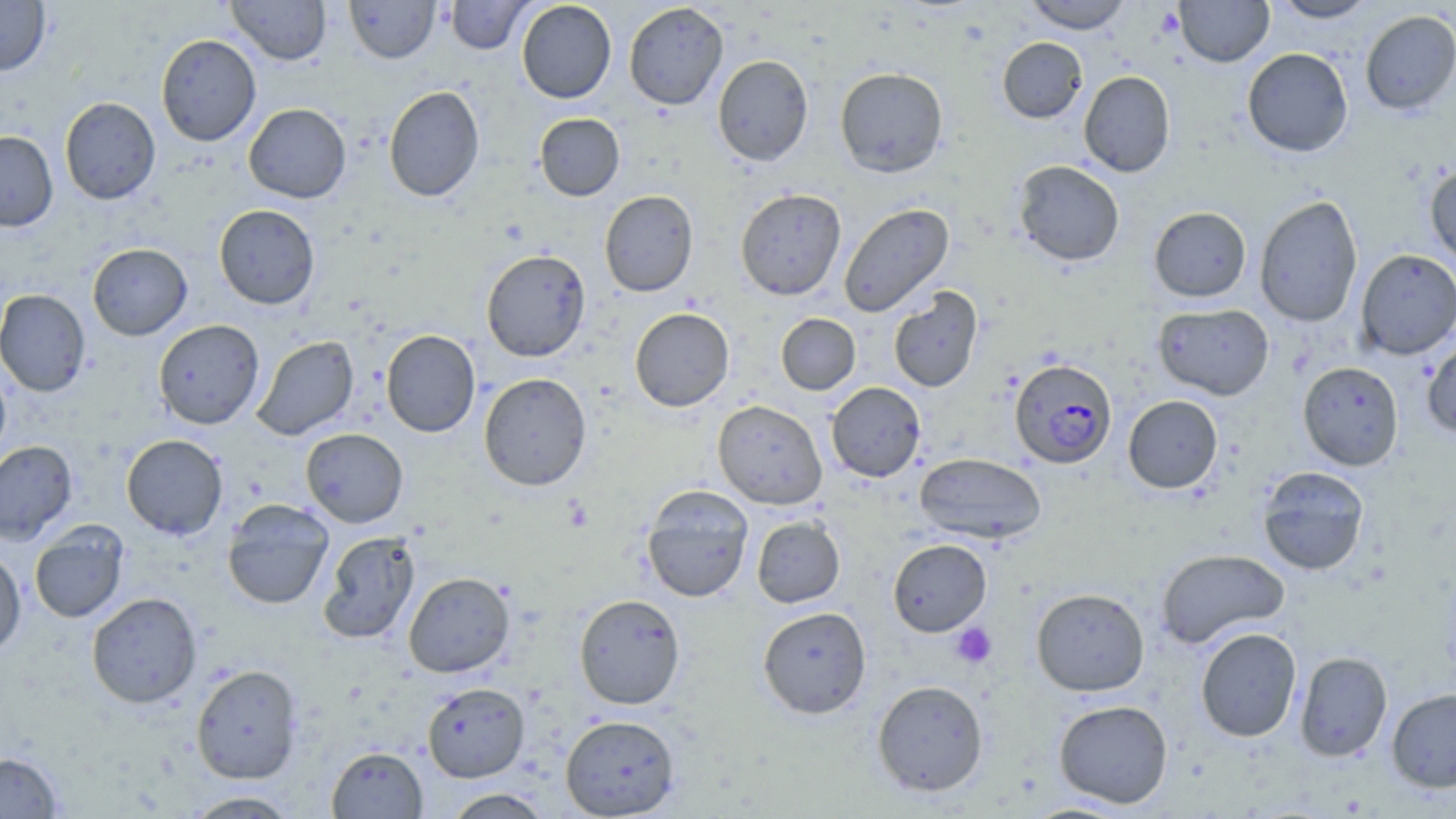
Summary:
  - Coordinate format: approximate bounding boxes as (x1,y1)-(x2,y2) corner pairs in pixels
  - Plasmodium falciparum-infected red blood cell locations: (1010,358)-(1117,468)
  - Platelet locations: (949,622)-(997,669)
  - Uninfected red blood cell locations: (0,0)-(51,75), (227,0)-(331,65), (344,0)-(441,63), (446,0)-(532,54), (1022,0)-(1132,33), (1174,0)-(1274,66), (1270,0)-(1379,22), (517,1)-(617,103), (623,2)-(729,110), (1360,10)-(1456,115), (156,34)-(261,146), (997,37)-(1088,123), (1242,47)-(1353,157), (713,55)-(813,167), (835,67)-(949,177), (1079,71)-(1175,177), (383,85)-(484,202), (59,97)-(161,204), (243,103)-(351,203), (534,113)-(624,201), (0,131)-(58,231), (1012,160)-(1125,266), (1425,162)-(1456,267), (735,188)-(846,300), (599,190)-(698,297), (1254,194)-(1363,328), (838,203)-(954,316), (214,204)-(320,309), (1149,206)-(1251,302), (87,243)-(192,340), (481,249)-(591,362), (1355,249)-(1456,359), (888,286)-(983,392), (0,289)-(91,397), (1153,303)-(1274,399), (629,307)-(734,412), (775,313)-(860,395), (153,319)-(264,429), (381,330)-(481,437), (251,335)-(359,440), (1422,338)-(1456,440), (0,361)-(12,465), (1298,361)-(1404,470), (479,373)-(591,490), (826,382)-(926,482), (1122,395)-(1223,493), (713,399)-(827,509), (300,428)-(408,527), (121,434)-(228,540), (0,440)-(78,545), (914,452)-(1047,544), (1257,466)-(1370,576), (641,485)-(754,602), (222,499)-(334,610), (751,516)-(845,608), (29,522)-(129,623), (318,531)-(419,645), (888,538)-(992,636), (1156,548)-(1290,649), (0,549)-(26,655), (403,572)-(515,677), (1031,587)-(1149,696), (86,592)-(202,707), (574,593)-(686,709), (757,606)-(872,718), (1195,627)-(1302,742), (1294,651)-(1392,761), (191,664)-(303,784), (872,679)-(989,797), (422,682)-(530,782), (1387,688)-(1456,792), (1054,699)-(1173,808), (560,714)-(680,818), (327,745)-(428,818), (0,751)-(63,818), (443,788)-(553,818), (183,790)-(299,818)
  - Slide-level diagnosis: Plasmodium falciparum
  - Image size: 1456×819 pixels
  - Field of view: single
  - Magnification: 1000x
  - Preparation: thin blood smear
  - Stain: May-Grünwald-Giemsa
  - Modality: light microscopy